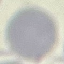

Malaria status: uninfected. Giemsa stain. Thin smear of blood. Automatically extracted cell patch, resized to 64 × 64 pixels. Acquired by smartphone through the microscope eyepiece.